Describe the morphology of the erythrocytes.
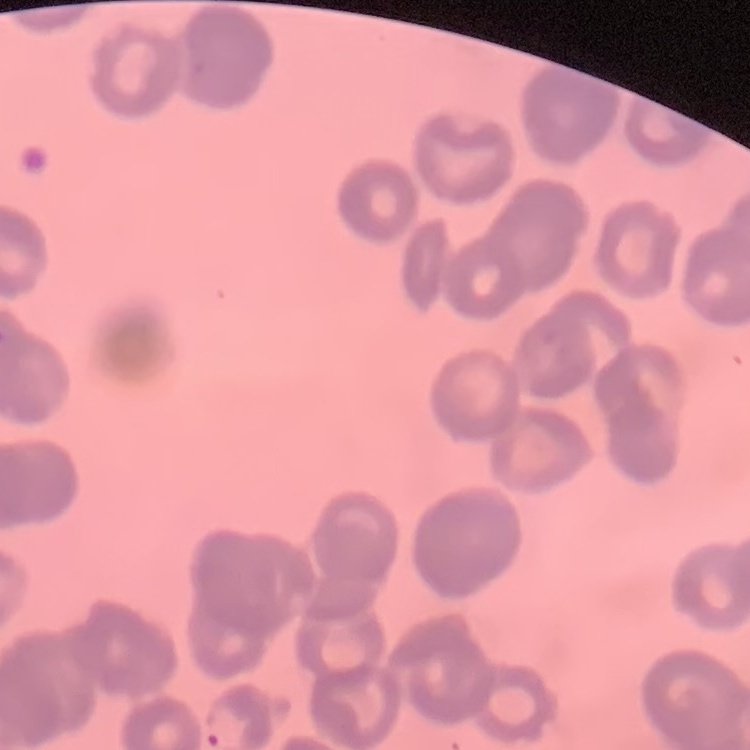
Rouleaux formation.

Thin blood film. Square crop of a larger photomicrograph. Stained with either Field's or Giemsa.